Assess this cell for malaria.
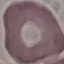
Uninfected.

image type = automatically extracted cell patch, resized to 64 × 64 pixels
stain = Giemsa
preparation = thin blood film
capture = smartphone through the microscope eyepiece